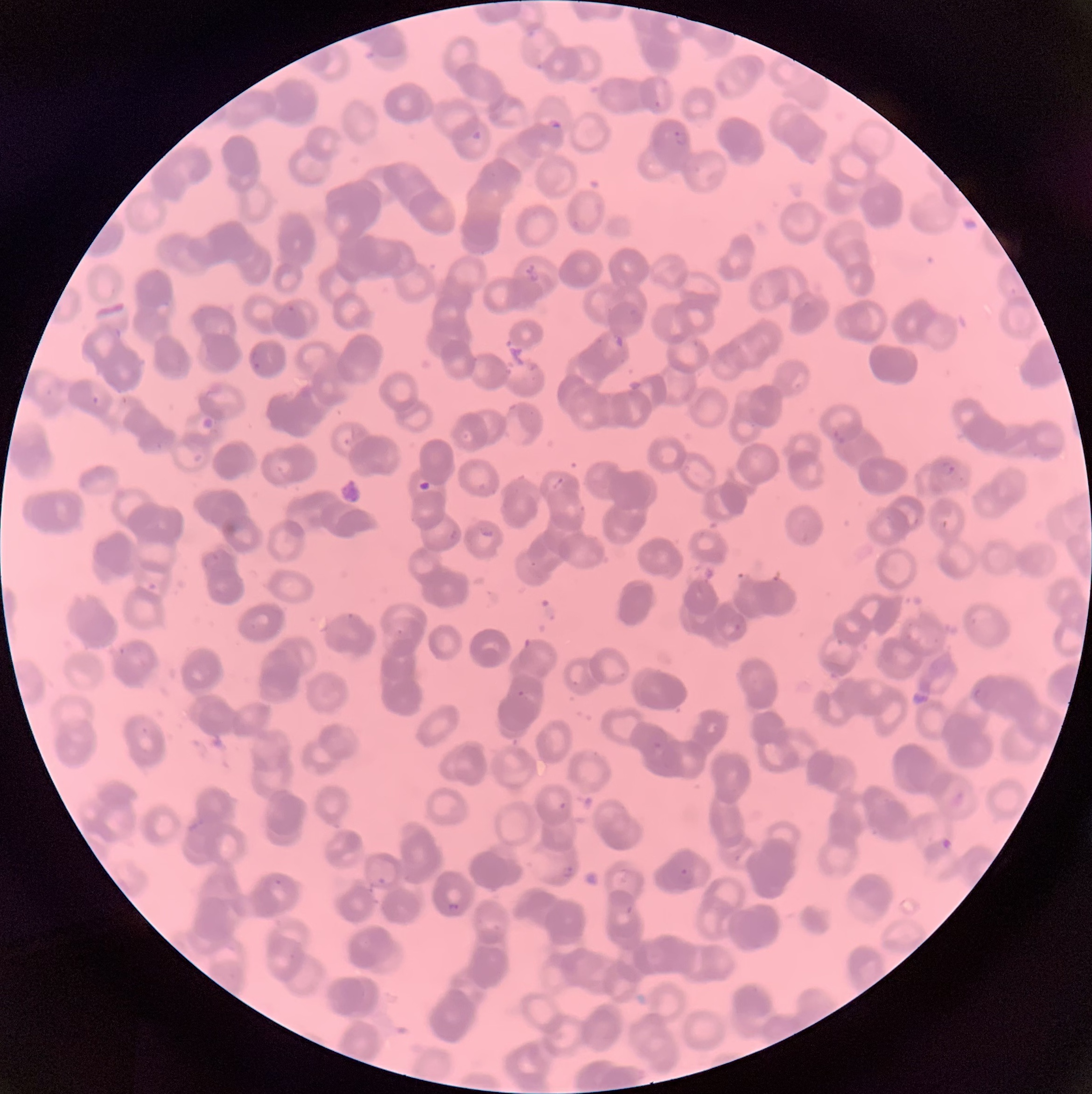
Approximate bounding boxes as (x1, y1, x2, y2) in pixels. Plasmodium parasite locations: (544, 116, 567, 135), (671, 130, 690, 149), (250, 351, 263, 370), (91, 395, 101, 406), (941, 461, 956, 476), (729, 614, 746, 633), (517, 690, 525, 698), (652, 740, 663, 750), (559, 800, 568, 811), (560, 864, 575, 879), (679, 867, 694, 884), (272, 877, 284, 888), (377, 877, 386, 887), (447, 902, 461, 914), (626, 905, 634, 915). Thin blood smear. Light microscopy. Image is 1092×1094 pixels. The red blood cells show rouleaux formation.